Locate and identify every blood parasite.
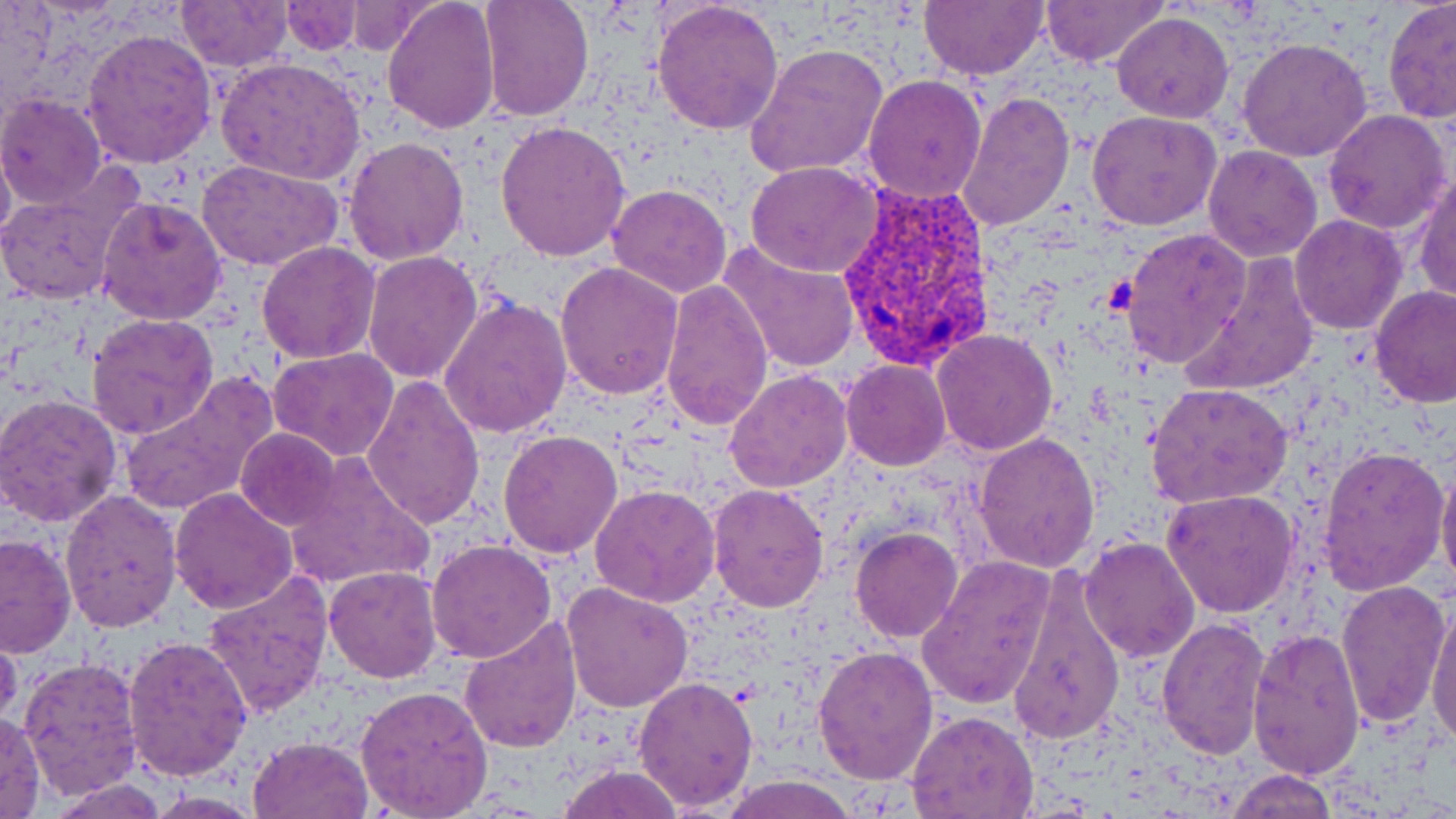

Approximate bounding boxes as (x1,y1)-(x2,y2) corner pairs in pixels.
Plasmodium vivax-infected red blood cells: (832,180)-(996,371).
No Plasmodium falciparum, Plasmodium ovale, Plasmodium malariae, Babesia divergens, or Trypanosoma brucei observed.

Summary:
  - Platelet locations: (1103,275)-(1136,314)
  - Uninfected red blood cell locations: (175,0)-(292,71), (383,0)-(501,135), (478,0)-(594,121), (652,0)-(785,137), (919,0)-(1047,80), (1039,0)-(1168,69), (1382,0)-(1456,123), (280,2)-(363,54), (341,2)-(441,55), (1112,12)-(1234,123), (82,27)-(218,169), (1237,36)-(1372,162), (744,43)-(889,180), (217,56)-(367,185), (862,75)-(988,203), (955,89)-(1074,235), (0,94)-(108,209), (1087,109)-(1222,229), (1323,109)-(1452,234), (494,120)-(631,261), (343,135)-(470,267), (1,140)-(15,253), (1203,145)-(1323,263), (199,159)-(342,273), (746,163)-(882,278), (0,170)-(140,308), (1411,170)-(1456,304), (616,182)-(744,426), (606,183)-(732,298), (97,194)-(227,324), (1290,214)-(1406,334), (1120,227)-(1251,369), (719,240)-(860,373), (256,241)-(382,364), (362,251)-(484,385), (1181,253)-(1323,397), (555,262)-(685,400), (660,279)-(774,431), (1369,284)-(1455,408), (438,296)-(571,439), (86,313)-(219,441), (931,329)-(1058,457), (269,348)-(400,463), (841,360)-(951,470), (725,369)-(854,493), (118,374)-(278,518), (364,376)-(484,530), (1146,384)-(1292,508), (0,391)-(124,528), (236,428)-(340,530), (497,428)-(622,559), (973,431)-(1101,571), (1317,444)-(1449,595), (282,451)-(436,592), (1436,461)-(1456,598), (707,482)-(831,612), (590,483)-(721,608), (169,487)-(297,613), (60,489)-(182,631), (1161,489)-(1300,618), (850,528)-(962,643), (0,533)-(76,659), (1078,536)-(1200,663), (427,538)-(557,663), (918,554)-(1057,711), (1009,565)-(1124,748), (323,566)-(444,684), (201,571)-(334,719), (1334,579)-(1450,729), (563,584)-(693,713), (1427,597)-(1456,752), (458,617)-(582,754), (1155,618)-(1271,758), (0,626)-(22,734), (1247,627)-(1367,780), (122,634)-(254,783), (813,645)-(940,785), (21,656)-(144,798), (633,675)-(760,813), (355,685)-(493,816), (0,710)-(47,818), (905,711)-(1039,819), (248,735)-(373,818), (556,764)-(690,819), (1227,770)-(1338,818), (718,775)-(858,818), (48,778)-(170,818), (142,793)-(270,817)
  - Slide-level diagnosis: Plasmodium vivax
  - Magnification: 1000x
  - Modality: optical microscopy
  - Image size: 1456×819 pixels
  - Preparation: thin blood smear
  - Stain: May-Grünwald-Giemsa
  - Field of view: single